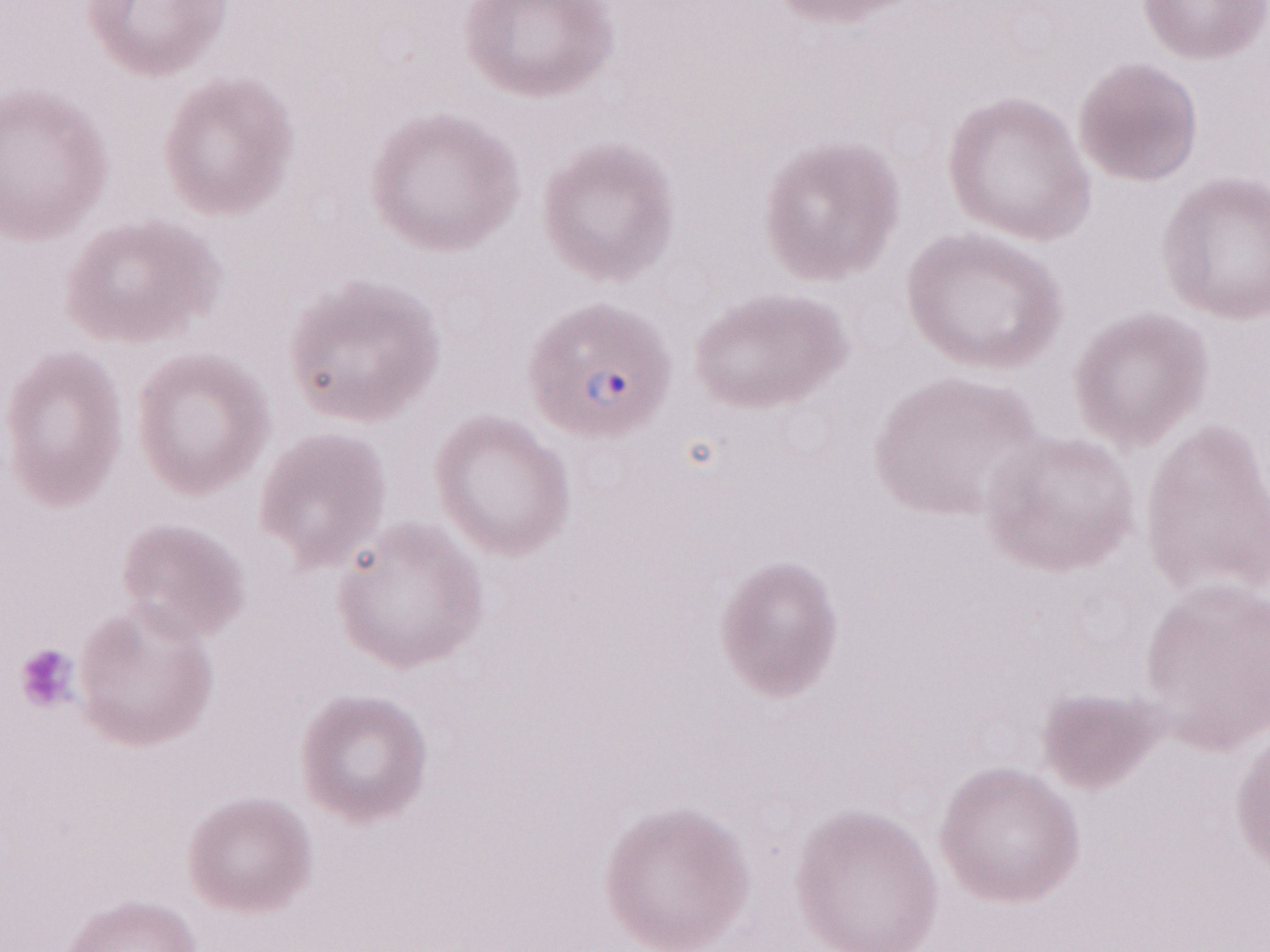

Single field of view. Image is 1270×952 pixels. Patient-level malaria diagnosis: positive. 1,000x magnification. Olympus BX43 microscope and DP73 digital camera. Thin peripheral-blood smear. May-Grünwald-Giemsa-stained preparation.